Classify this cell by malaria status.
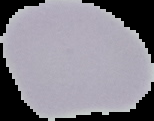

It is uninfected.

Segmented cell region on a black background. Image is 154×121 pixels. From a thin blood film.